Comment on the morphology of the red blood cells.
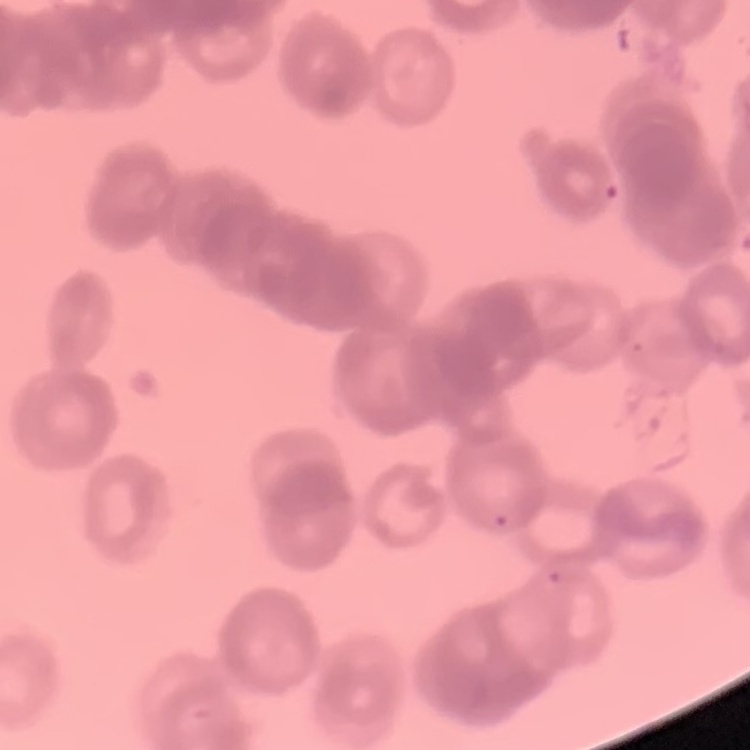

Rouleaux formation.

Stained with either Field's or Giemsa. Square crop of a larger photomicrograph. Thin peripheral smear.